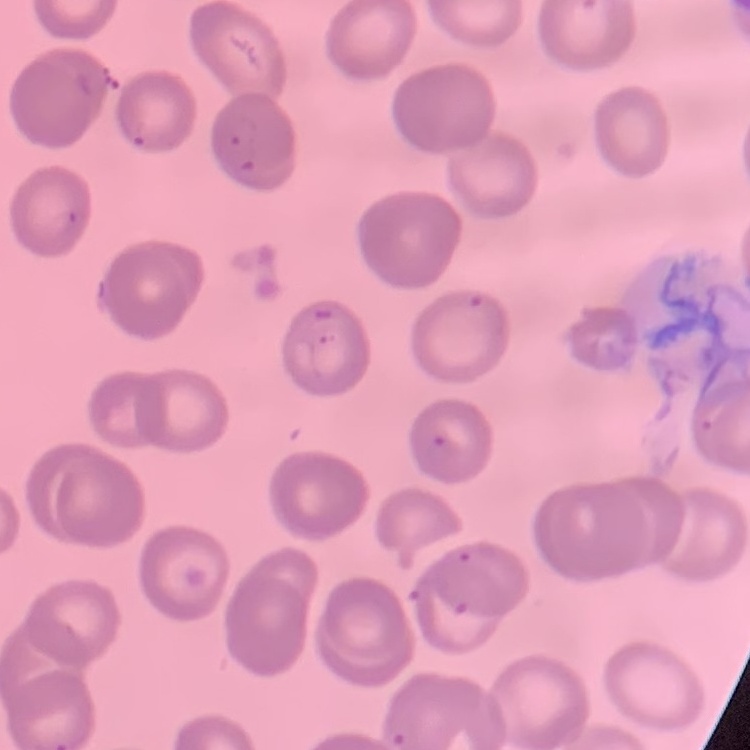
Summary:
  - Red blood cell morphology: no rouleaux formation
  - Stain: Field's or Giemsa
  - Preparation: thin blood smear
  - Image type: square crop of a larger photomicrograph